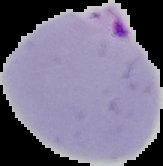
From a thin blood smear. Cell region segmented out of the field of view; the surrounding area is masked to black. Result: Plasmodium parasites detected. Image is 163×166 pixels.